Evaluate for parasitized red blood cells.
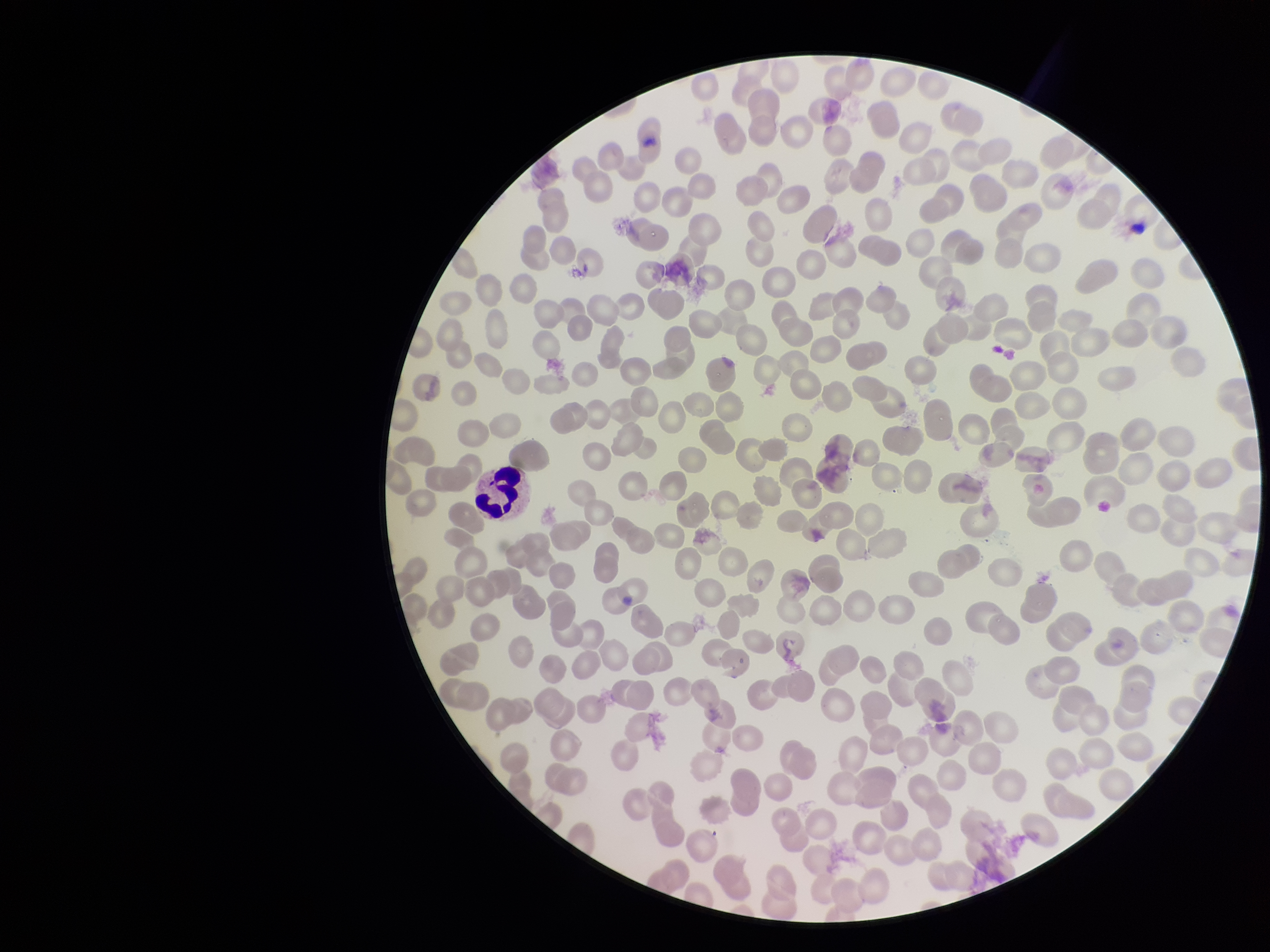

None seen.

Summary:
  - Patient malaria status: negative
  - Capture: smartphone photograph through the microscope eyepiece
  - Image size: 1270×952 pixels
  - Stain: Giemsa
  - Field of view: single
  - Preparation: thin smear
  - Red blood cell count: 278
  - Parasitized red blood cell count: 0